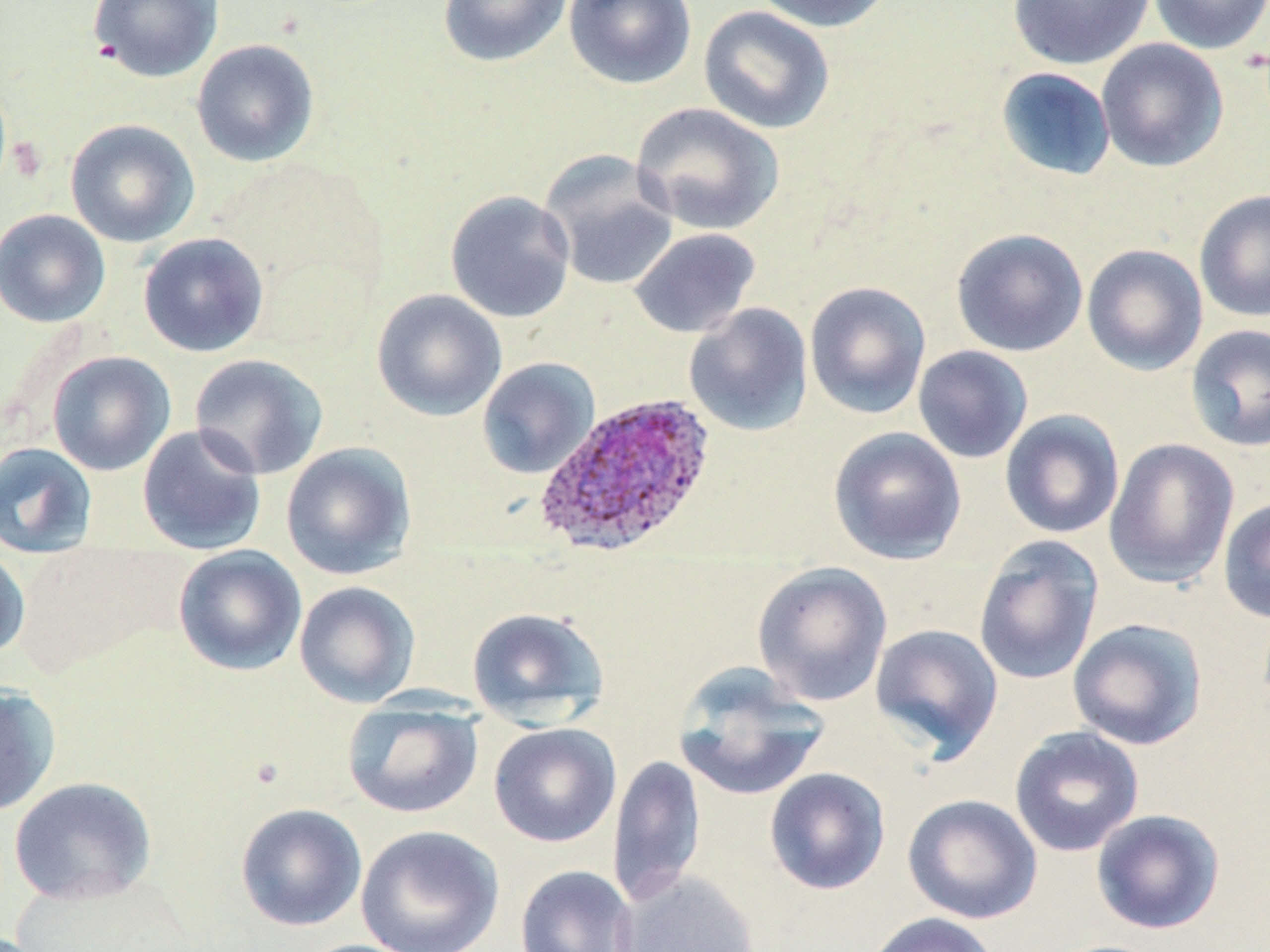
Summary:
  - Coordinate format: approximate bounding boxes as named x1/y1/x2/y2 corners in pixels
  - Plasmodium ovale-infected red blood cell locations: (x1=534, y1=393, x2=717, y2=558)
  - Uninfected red blood cell locations: (x1=87, y1=0, x2=223, y2=83), (x1=437, y1=0, x2=573, y2=68), (x1=563, y1=0, x2=697, y2=90), (x1=751, y1=0, x2=896, y2=33), (x1=1007, y1=0, x2=1156, y2=70), (x1=1150, y1=0, x2=1270, y2=54), (x1=698, y1=5, x2=836, y2=134), (x1=1095, y1=38, x2=1229, y2=173), (x1=191, y1=39, x2=320, y2=167), (x1=996, y1=67, x2=1116, y2=181), (x1=630, y1=102, x2=784, y2=236), (x1=64, y1=119, x2=200, y2=248), (x1=540, y1=151, x2=679, y2=291), (x1=1193, y1=188, x2=1270, y2=323), (x1=445, y1=190, x2=576, y2=323), (x1=0, y1=208, x2=111, y2=328), (x1=629, y1=227, x2=761, y2=339), (x1=951, y1=228, x2=1088, y2=357), (x1=137, y1=232, x2=269, y2=357), (x1=1081, y1=244, x2=1208, y2=377), (x1=804, y1=281, x2=931, y2=420), (x1=371, y1=289, x2=507, y2=421), (x1=683, y1=303, x2=814, y2=437), (x1=1185, y1=323, x2=1270, y2=451), (x1=912, y1=345, x2=1033, y2=464), (x1=47, y1=351, x2=176, y2=476), (x1=189, y1=353, x2=329, y2=479), (x1=477, y1=358, x2=599, y2=479), (x1=1000, y1=409, x2=1125, y2=539), (x1=137, y1=424, x2=267, y2=556), (x1=828, y1=426, x2=967, y2=565), (x1=1103, y1=438, x2=1239, y2=589), (x1=0, y1=442, x2=98, y2=558), (x1=281, y1=442, x2=417, y2=580), (x1=1218, y1=497, x2=1270, y2=623), (x1=973, y1=536, x2=1104, y2=686), (x1=173, y1=544, x2=307, y2=677), (x1=0, y1=545, x2=30, y2=661), (x1=751, y1=562, x2=893, y2=707), (x1=293, y1=581, x2=420, y2=708), (x1=466, y1=606, x2=609, y2=728), (x1=1067, y1=617, x2=1209, y2=751), (x1=870, y1=623, x2=1004, y2=762), (x1=673, y1=664, x2=831, y2=802), (x1=0, y1=684, x2=62, y2=816), (x1=342, y1=700, x2=484, y2=819), (x1=488, y1=722, x2=622, y2=848), (x1=1009, y1=725, x2=1145, y2=857), (x1=608, y1=753, x2=706, y2=907), (x1=764, y1=767, x2=891, y2=895), (x1=8, y1=776, x2=157, y2=906), (x1=903, y1=793, x2=1042, y2=924), (x1=235, y1=802, x2=367, y2=932), (x1=1090, y1=808, x2=1226, y2=935), (x1=355, y1=824, x2=504, y2=952), (x1=514, y1=864, x2=638, y2=952), (x1=615, y1=870, x2=761, y2=952), (x1=862, y1=912, x2=999, y2=952), (x1=292, y1=938, x2=427, y2=952)
  - Slide-level diagnosis: Plasmodium ovale
  - Modality: light microscopy
  - Preparation: thin blood film
  - Field of view: single
  - Image size: 1270×952 pixels
  - Stain: May-Grünwald-Giemsa
  - Magnification: 1000x